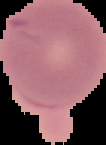

{
  "image_type": "segmented cell region on a black background",
  "result": "no malaria parasites seen",
  "preparation": "thin blood smear",
  "image_size": "106×145 pixels"
}